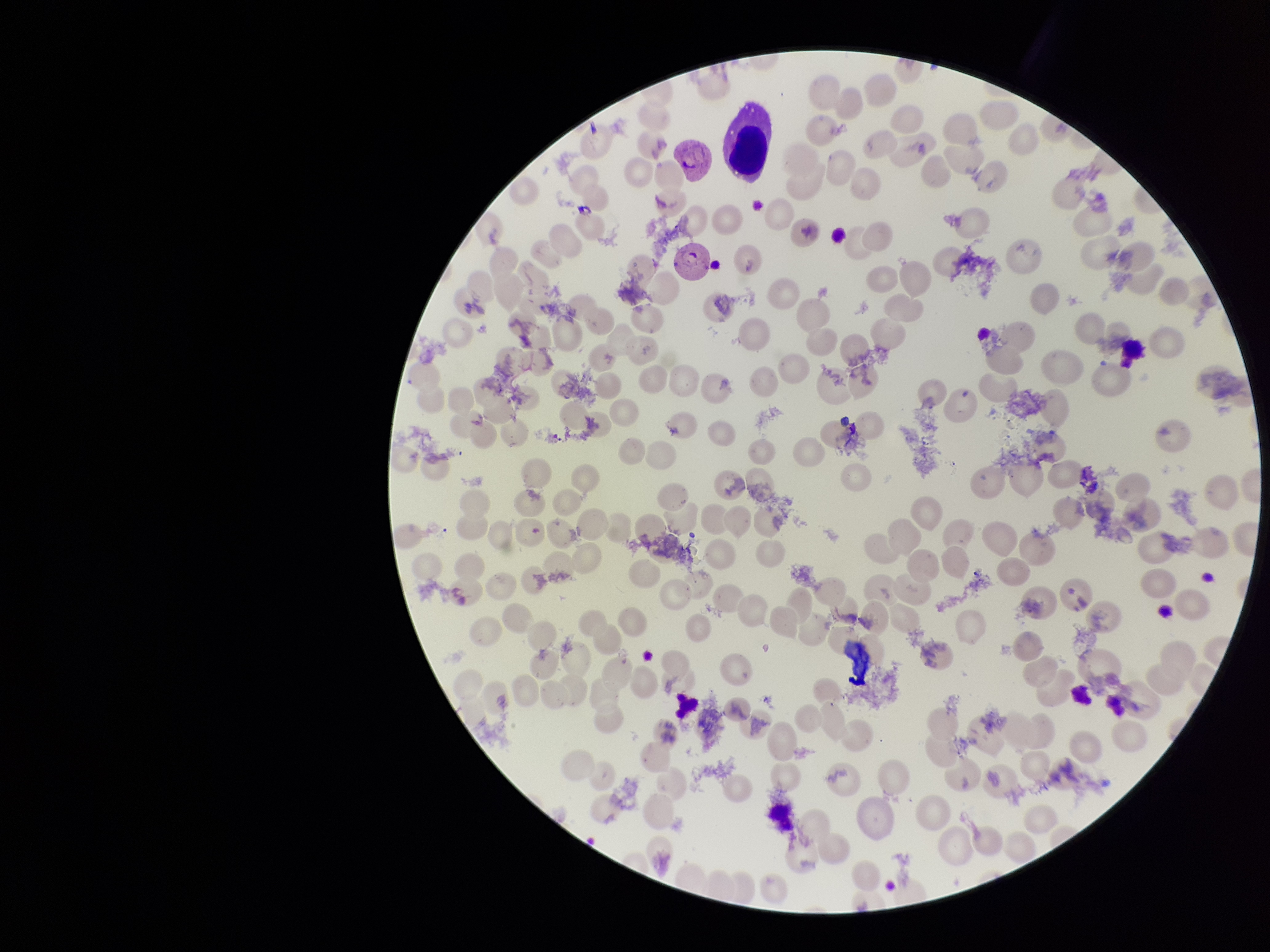
Summary:
  - Stain: Giemsa
  - Preparation: thin blood smear
  - Parasitized red blood cells: none seen
  - Field of view: single
  - Species reported for this patient: Plasmodium vivax
  - Image size: 1270×952 pixels
  - Parasitized red blood cell count: 0
  - Patient malaria status: positive
  - Capture: smartphone photograph through the microscope eyepiece
  - Red blood cell count: 90